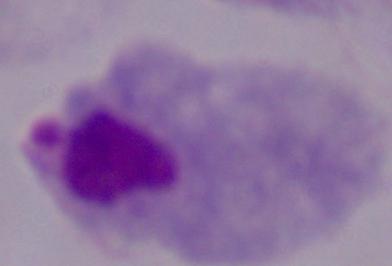
modality = micrograph
magnification = 1000x
identification = trichomonad